Identify the blood parasite species.
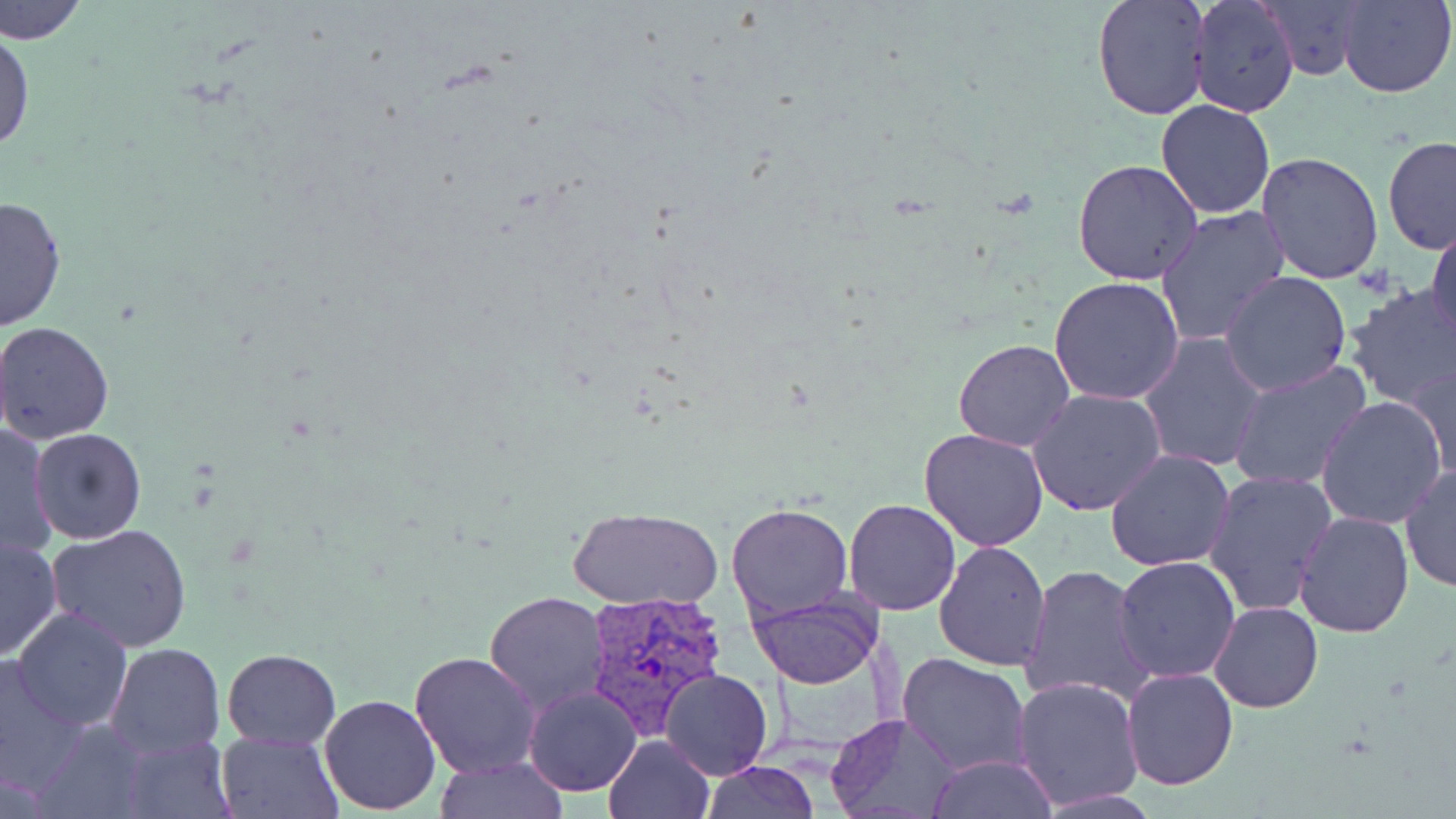

Plasmodium vivax.

stain = May-Grünwald-Giemsa
modality = light microscopy
uninfected red blood cell locations = approximate bounding boxes as (x1, y1, x2, y2) in pixels: (0, 0, 88, 47), (1092, 0, 1212, 122), (1189, 0, 1300, 118), (1259, 0, 1373, 81), (1338, 1, 1455, 98), (0, 23, 35, 158), (1155, 100, 1277, 220), (1382, 136, 1456, 255), (1257, 153, 1385, 285), (1073, 159, 1203, 284), (0, 194, 69, 331), (1156, 206, 1291, 347), (1426, 223, 1456, 348), (1220, 269, 1352, 395), (1049, 277, 1184, 406), (1341, 285, 1456, 410), (1, 321, 117, 444), (1138, 332, 1267, 472), (952, 339, 1076, 452), (1227, 361, 1371, 491), (1404, 361, 1456, 483), (1029, 388, 1169, 517), (1315, 397, 1448, 529), (0, 423, 57, 563), (919, 427, 1050, 551), (30, 428, 146, 543), (1104, 449, 1236, 572), (1399, 466, 1456, 592), (1203, 471, 1336, 619), (844, 499, 962, 617), (725, 501, 853, 620), (568, 508, 723, 610), (1294, 512, 1414, 638), (47, 524, 193, 651), (0, 536, 62, 661), (933, 540, 1052, 669), (1113, 556, 1240, 684), (1019, 564, 1157, 707), (749, 589, 881, 689), (483, 590, 608, 713), (1210, 600, 1322, 712), (11, 608, 133, 732), (105, 643, 225, 758), (222, 647, 340, 749), (409, 650, 542, 779), (0, 651, 92, 797), (898, 653, 1031, 776), (1121, 667, 1238, 790), (660, 669, 771, 779), (1013, 676, 1145, 811), (523, 685, 643, 797), (319, 692, 442, 816), (31, 713, 152, 819), (828, 713, 960, 819), (216, 731, 342, 818), (116, 734, 235, 819), (603, 734, 715, 819), (927, 756, 1059, 818), (433, 757, 570, 817), (702, 762, 820, 819)
preparation = thin blood film
image size = 1456×819 pixels
Plasmodium vivax-infected red blood cell locations = approximate bounding boxes as (x1, y1, x2, y2) in pixels: (581, 588, 732, 735)
field of view = single
magnification = 1000x